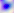

Summary:
  - Identification: Toxoplasma gondii
  - Modality: micrograph
  - Magnification: 400x